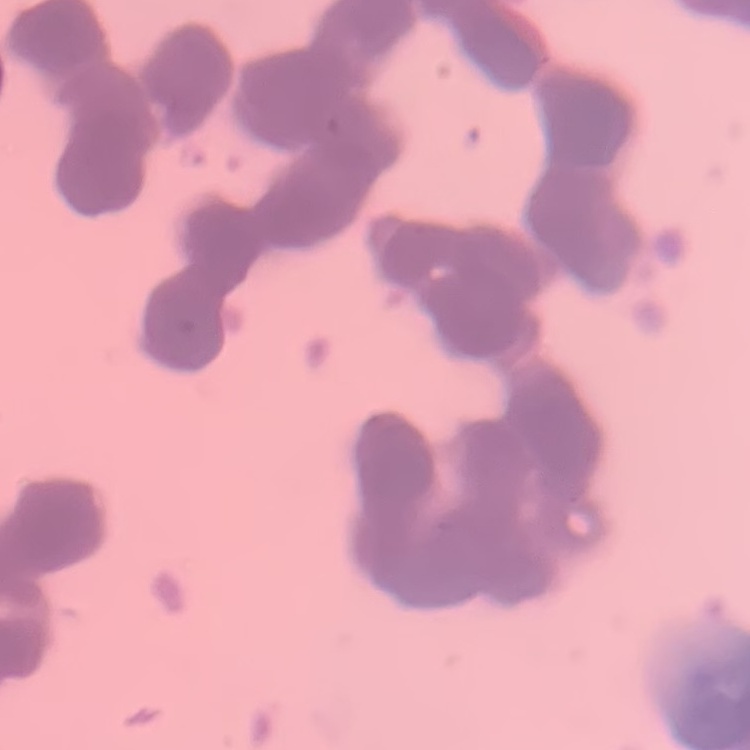
erythrocyte morphology = rouleaux formation
image type = one tile cut from a larger photomicrograph
preparation = thin blood smear
stain = Field's or Giemsa